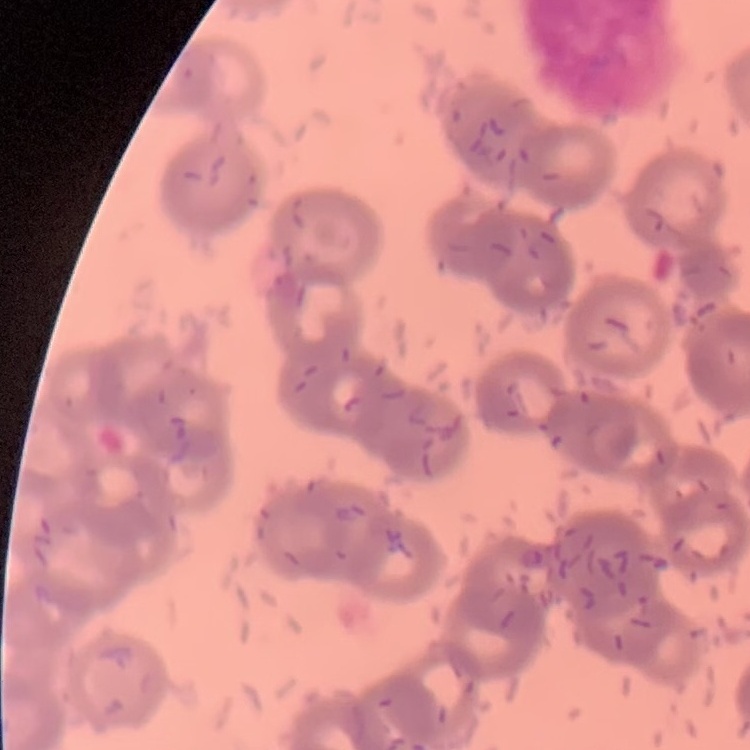

The red blood cells show rouleaux formation. Square crop of a larger photomicrograph. Field's or Giemsa stain. Thin peripheral smear.